Locate every Plasmodium parasite.
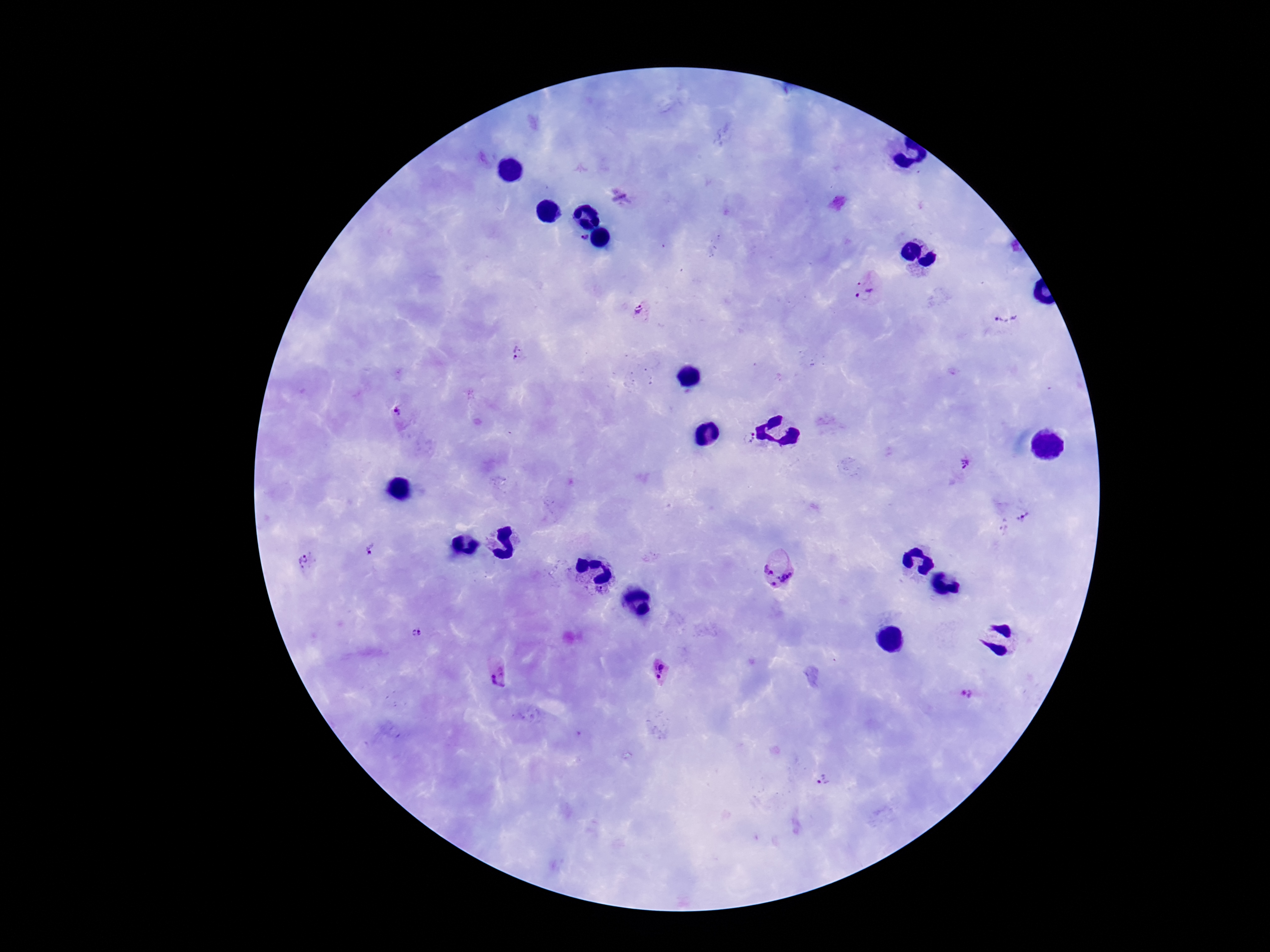

Approximate centers as (x, y) in pixels.
Plasmodium parasites: (580, 241), (863, 288), (645, 310), (1002, 316), (521, 355), (397, 411), (746, 437), (966, 465), (1025, 516), (371, 549), (307, 562), (781, 569), (415, 632), (499, 672), (661, 672), (970, 692), (822, 781).

Photographed through the microscope eyepiece with a smartphone camera. Image is 1270×952 pixels. Giemsa stain. Thick blood smear. One field from this slide. 100x magnification. Patient malaria status: infected.